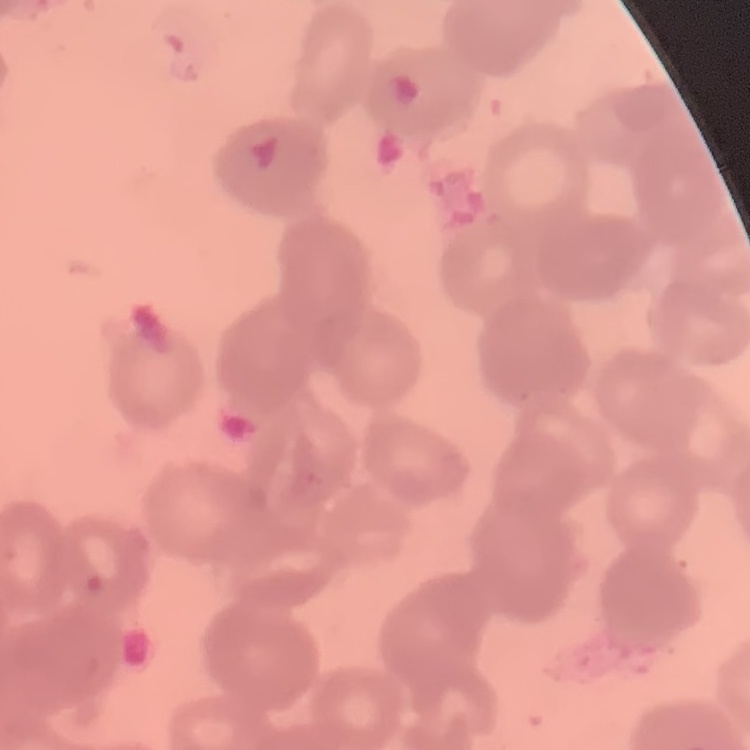
Summary:
  - Red blood cell morphology: rouleaux formation
  - Preparation: thin blood smear
  - Stain: Field's or Giemsa
  - Image type: one tile cut from a larger photomicrograph